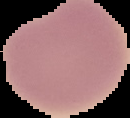

Image is 130×118 pixels. From a thin blood film. The area outside the segmented cell region is set to black. Malaria status: uninfected.